Name the cell type shown.
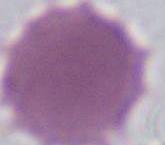
This is an erythrocyte.

Photomicrograph. Captured at 1000x magnification.